Locate and identify every blood parasite.
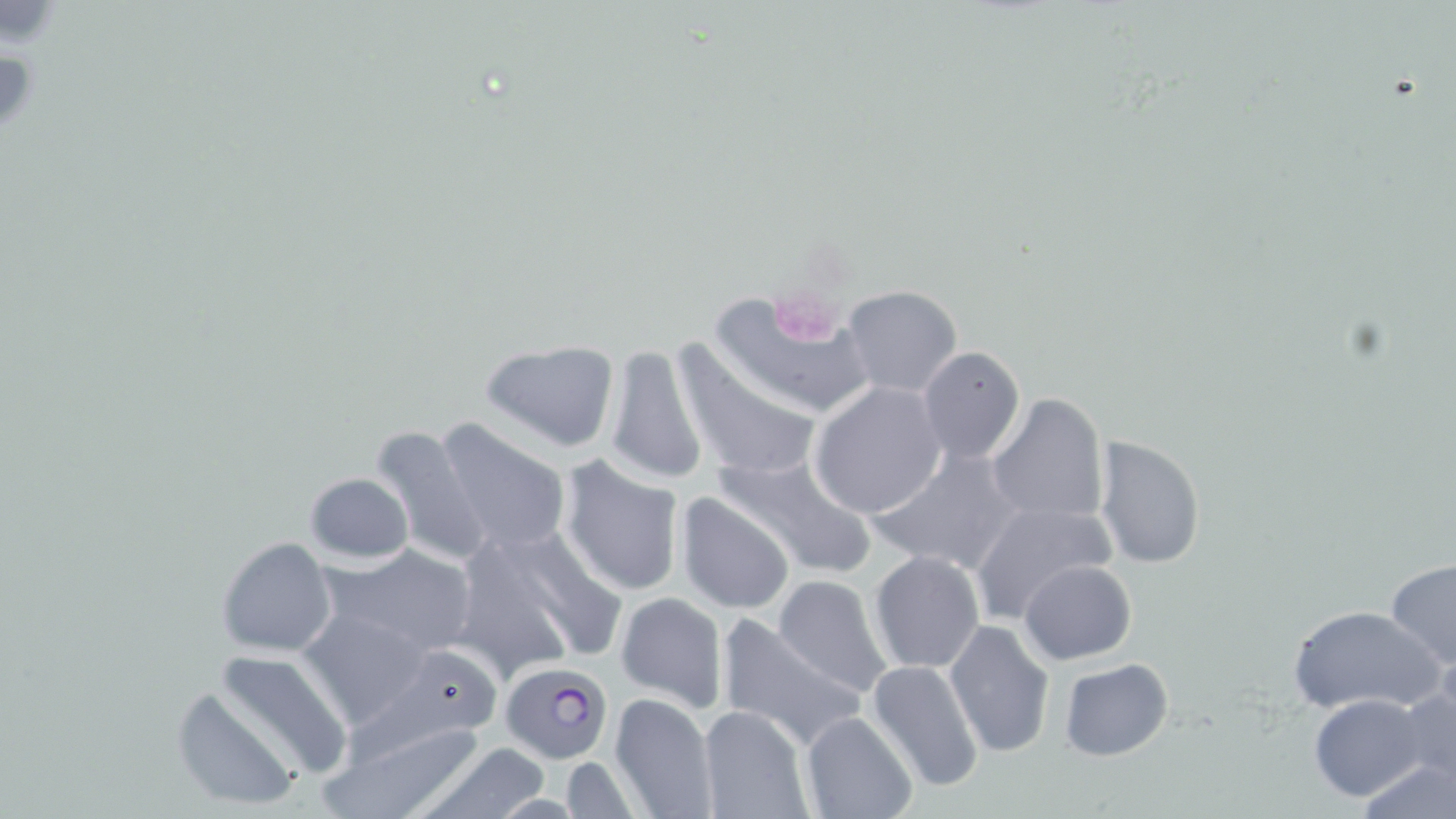
Approximate bounding boxes as (x1, y1, x2, y2) in pixels.
Plasmodium falciparum-infected red blood cells: (499, 662, 613, 762).
No Plasmodium ovale, Plasmodium malariae, Plasmodium vivax, Babesia divergens, or Trypanosoma brucei observed.

slide-level diagnosis = Plasmodium falciparum
stain = May-Grünwald-Giemsa
image size = 1456×819 pixels
modality = light microscopy
uninfected red blood cell locations = approximate bounding boxes as (x1, y1, x2, y2) in pixels: (840, 285, 963, 399), (710, 288, 874, 421), (478, 338, 622, 453), (669, 338, 825, 487), (601, 344, 710, 487), (917, 348, 1027, 464), (809, 382, 949, 518), (986, 392, 1111, 528), (434, 418, 574, 555), (367, 424, 491, 566), (1092, 435, 1207, 569), (868, 445, 1021, 576), (713, 449, 879, 579), (557, 456, 687, 598), (304, 472, 414, 565), (676, 493, 796, 614), (967, 500, 1117, 624), (448, 522, 618, 679), (216, 536, 338, 658), (320, 542, 479, 657), (869, 550, 986, 674), (1384, 558, 1456, 670), (1020, 560, 1136, 664), (772, 574, 895, 698), (616, 592, 728, 712), (1286, 604, 1444, 717), (295, 608, 433, 732), (715, 614, 864, 751), (944, 619, 1055, 760), (389, 644, 502, 737), (211, 649, 353, 780), (1057, 657, 1174, 761), (865, 660, 985, 795), (1398, 682, 1456, 787), (171, 685, 303, 812), (609, 692, 718, 819), (1308, 694, 1427, 801), (697, 704, 815, 819), (321, 712, 488, 818), (801, 712, 918, 819), (413, 742, 554, 819), (1358, 754, 1453, 819), (559, 756, 641, 819)
platelet locations = approximate bounding boxes as (x1, y1, x2, y2) in pixels: (780, 304, 841, 347)
preparation = thin blood film
magnification = 1000x
field of view = single